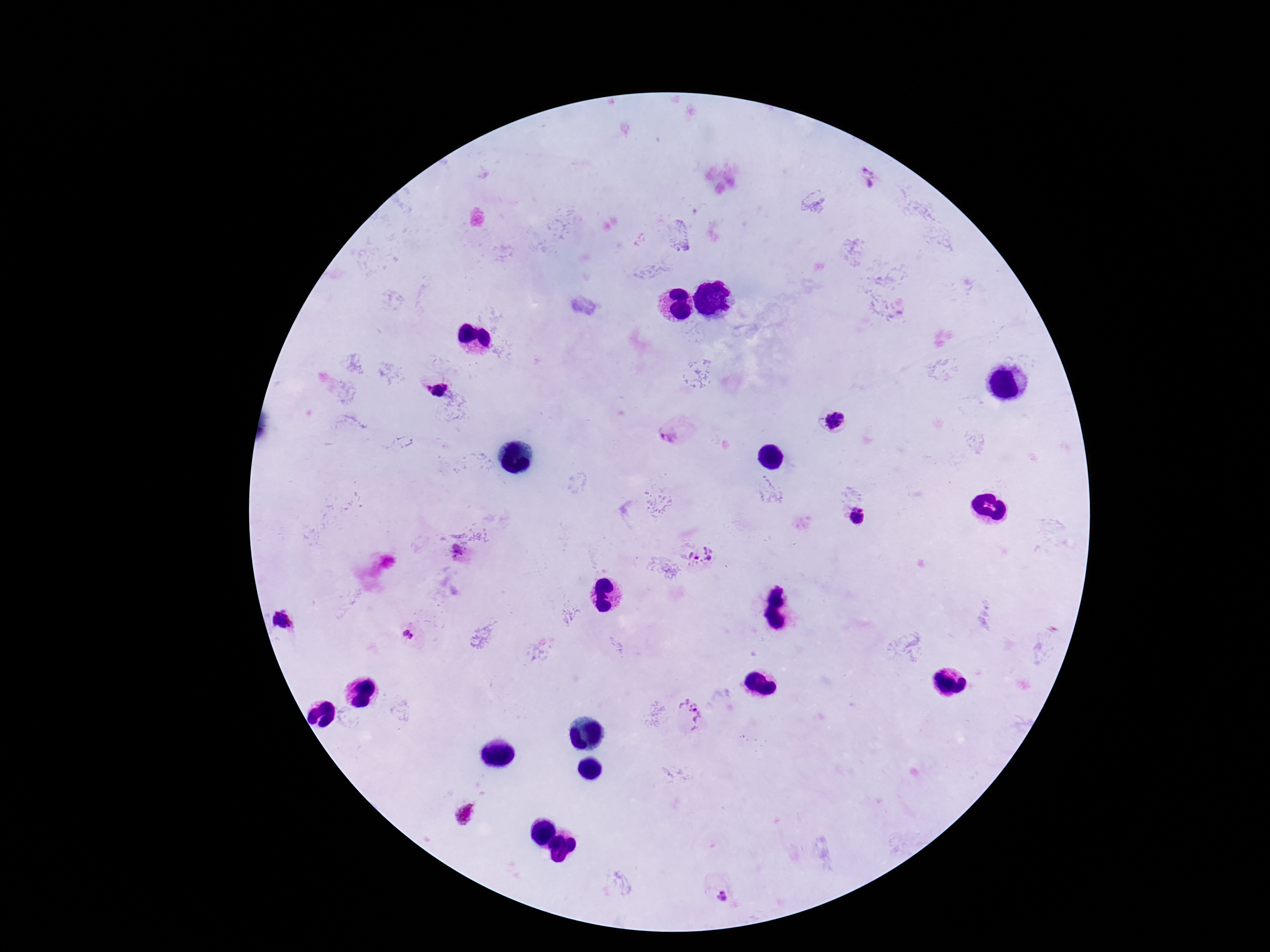 Approximate centers as [x, y] in pixels. Plasmodium parasite locations: [867, 177], [437, 389], [832, 420], [670, 435], [858, 517], [460, 554], [699, 557], [408, 634], [689, 713], [466, 813], [722, 901]. One field from this slide. Smartphone photograph taken through the microscope eyepiece. Thick blood smear. 100x magnification. Image is 1270×952 pixels. Patient malaria status: positive. Giemsa stain.